Assess this cell for malaria.
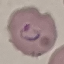

It is parasitized.

Summary:
  - Preparation: thin blood smear
  - Image type: automatically extracted cell patch, resized to 64 × 64 pixels
  - Capture: smartphone camera at the microscope eyepiece
  - Stain: Giemsa